Classify this cell by malaria status.
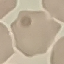

It is uninfected.

{
  "capture": "smartphone camera at the microscope eyepiece",
  "preparation": "thin blood film",
  "stain": "Giemsa",
  "image_type": "cell patch, automatically extracted from a larger field of view and resized to 64 × 64 pixels"
}